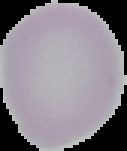

image size = 127×151 pixels
image type = cell region segmented out of the field of view; surrounding area masked to black
result = negative for Plasmodium parasites
preparation = thin blood smear